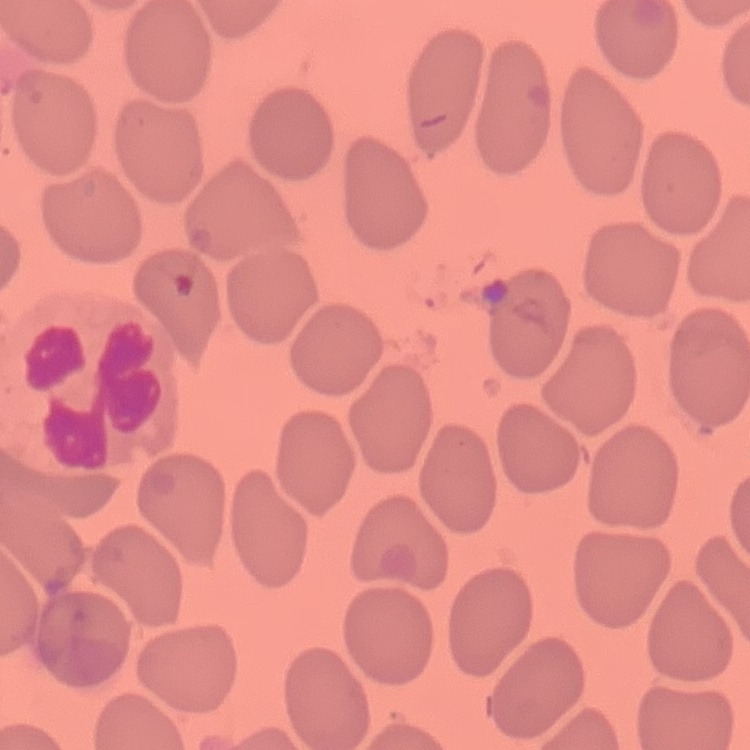

Summary:
  - Red blood cell morphology: no rouleaux formation
  - Image type: one tile cut from a larger photomicrograph
  - Preparation: thin peripheral smear
  - Stain: Field's or Giemsa